Identify the blood parasite species.
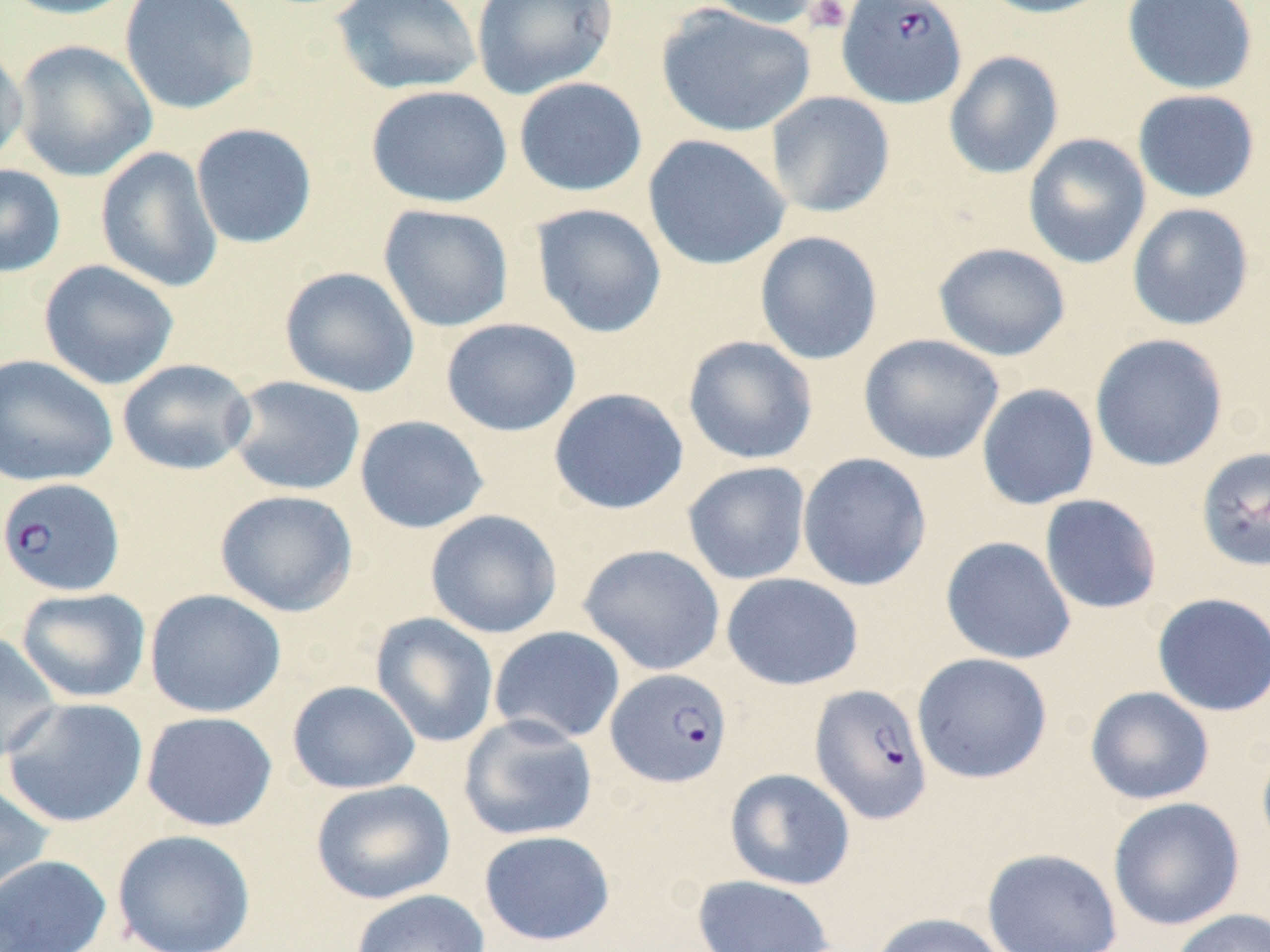

Plasmodium falciparum.

{
  "magnification": "1000x",
  "uninfected_red_blood_cell_locations": "approximate bounding boxes as (x1, y1, x2, y2) in pixels: (0, 0, 140, 20), (119, 0, 259, 115), (330, 0, 483, 96), (698, 0, 828, 29), (975, 0, 1117, 19), (1121, 0, 1259, 95), (470, 1, 619, 99), (655, 4, 815, 138), (12, 39, 157, 182), (0, 40, 29, 172), (943, 50, 1064, 180), (513, 76, 648, 197), (366, 85, 512, 208), (1132, 89, 1261, 203), (765, 91, 895, 218), (190, 123, 318, 249), (1023, 133, 1151, 269), (642, 134, 791, 271), (95, 146, 223, 293), (0, 164, 66, 278), (1127, 202, 1254, 331), (378, 203, 514, 332), (530, 203, 668, 339), (754, 231, 884, 365), (932, 242, 1072, 362), (38, 259, 180, 390), (279, 266, 420, 398), (441, 318, 581, 437), (858, 333, 1005, 464), (1090, 333, 1229, 472), (682, 335, 819, 465), (0, 354, 118, 488), (117, 359, 256, 476), (226, 375, 366, 496), (976, 383, 1100, 510), (548, 387, 689, 515), (354, 415, 490, 534), (797, 452, 932, 592), (682, 461, 811, 585), (214, 489, 358, 617), (1039, 494, 1163, 615), (425, 509, 563, 639), (940, 536, 1077, 665), (578, 543, 726, 676), (721, 572, 864, 691), (16, 587, 151, 703), (144, 588, 286, 718), (1152, 592, 1270, 717), (370, 612, 499, 748), (488, 626, 626, 745), (0, 633, 62, 764), (911, 652, 1052, 784), (286, 680, 421, 794), (1084, 686, 1215, 805), (2, 697, 149, 828), (141, 711, 278, 832), (459, 714, 598, 842), (1256, 737, 1270, 862), (725, 767, 856, 890), (310, 779, 456, 905), (0, 781, 54, 909), (1108, 797, 1245, 931), (112, 829, 256, 952), (479, 830, 615, 945), (982, 848, 1122, 952), (0, 854, 111, 952), (692, 874, 836, 952), (350, 889, 490, 952), (1168, 908, 1270, 952), (869, 912, 1010, 952)",
  "preparation": "thin blood smear",
  "modality": "light microscopy",
  "plasmodium_falciparum_infected_red_blood_cell_locations": "approximate bounding boxes as (x1, y1, x2, y2) in pixels: (836, 0, 967, 108), (1196, 446, 1269, 571), (0, 477, 125, 596), (605, 668, 733, 787), (809, 683, 932, 825)",
  "stain": "May-Grünwald-Giemsa",
  "field_of_view": "one of a larger specimen",
  "platelet_locations": "approximate bounding boxes as (x1, y1, x2, y2) in pixels: (804, 0, 853, 34)",
  "image_size": "1270×952 pixels"
}